Give the position of every Plasmodium parasite visible.
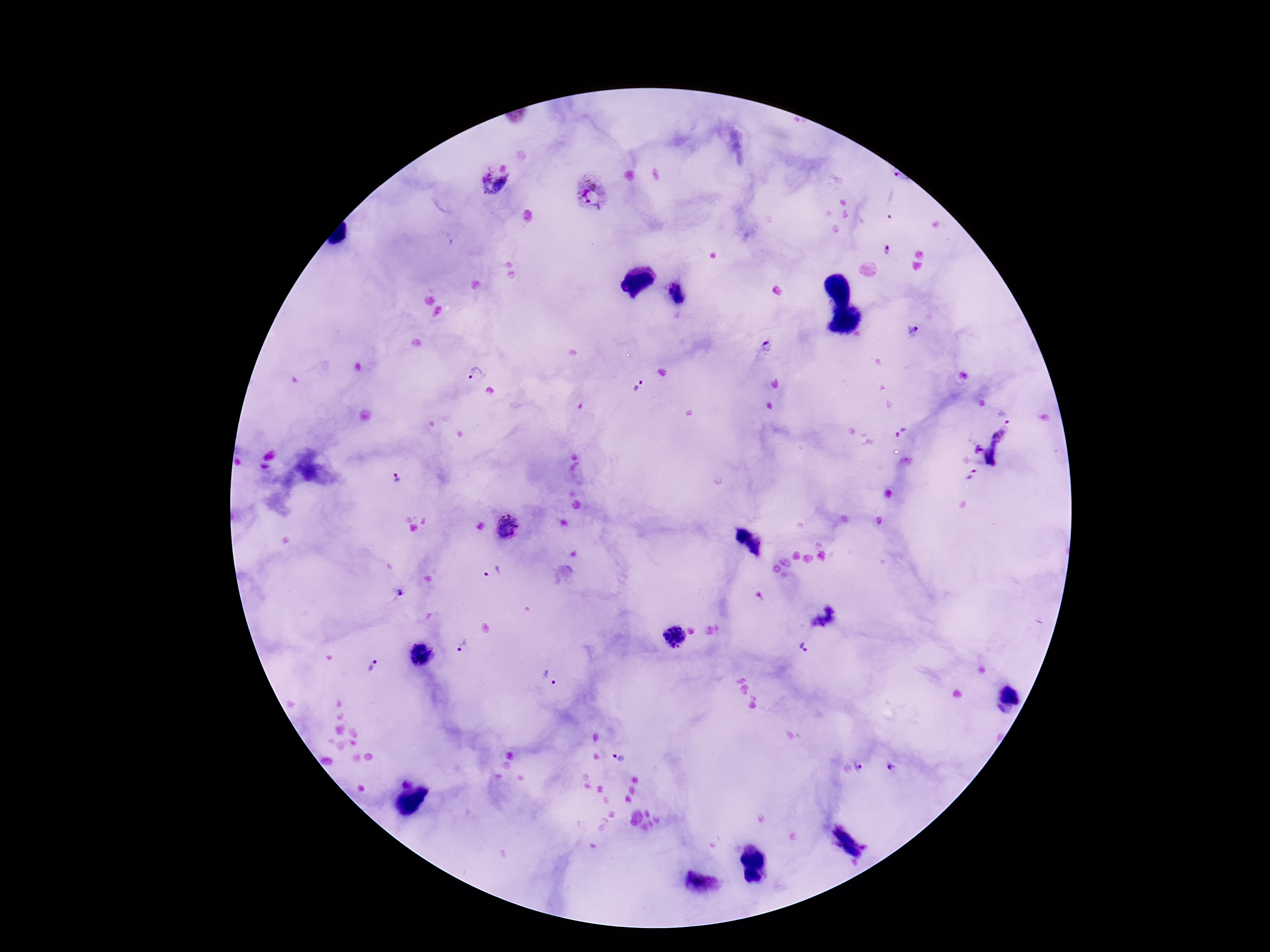

Approximate object centers, in pixels from the top-left corner.
Plasmodium parasites: (x=898, y=176), (x=491, y=186), (x=591, y=195), (x=896, y=206), (x=886, y=251), (x=912, y=334), (x=764, y=347), (x=476, y=373), (x=637, y=384), (x=1002, y=430), (x=978, y=450), (x=993, y=457), (x=973, y=476), (x=394, y=477), (x=509, y=526), (x=493, y=572), (x=400, y=593), (x=674, y=636), (x=464, y=646), (x=805, y=648), (x=421, y=655), (x=371, y=666), (x=549, y=678), (x=618, y=759), (x=860, y=767), (x=892, y=767).

Summary:
  - Patient malaria status: positive
  - Image size: 1270×952 pixels
  - Field of view: single
  - Capture: smartphone camera through the microscope eyepiece
  - Stain: Giemsa
  - Preparation: thick peripheral-blood smear
  - Magnification: 100x